Assess the morphology of the erythrocytes.
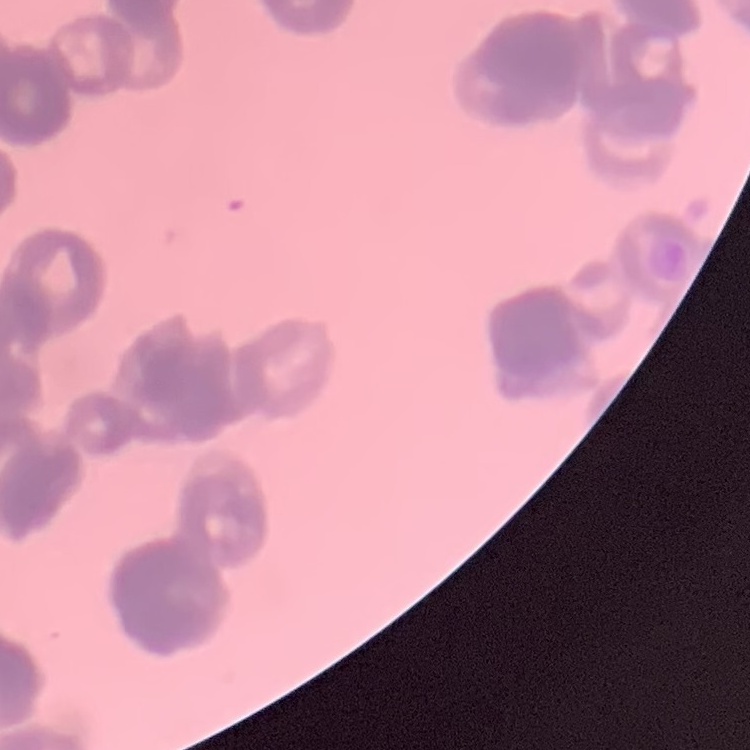
Rouleaux formation.

Summary:
  - Preparation: thin peripheral smear
  - Stain: Field's or Giemsa
  - Image type: one tile cut from a larger photomicrograph